Outline each Plasmodium falciparum-infected red blood cell.
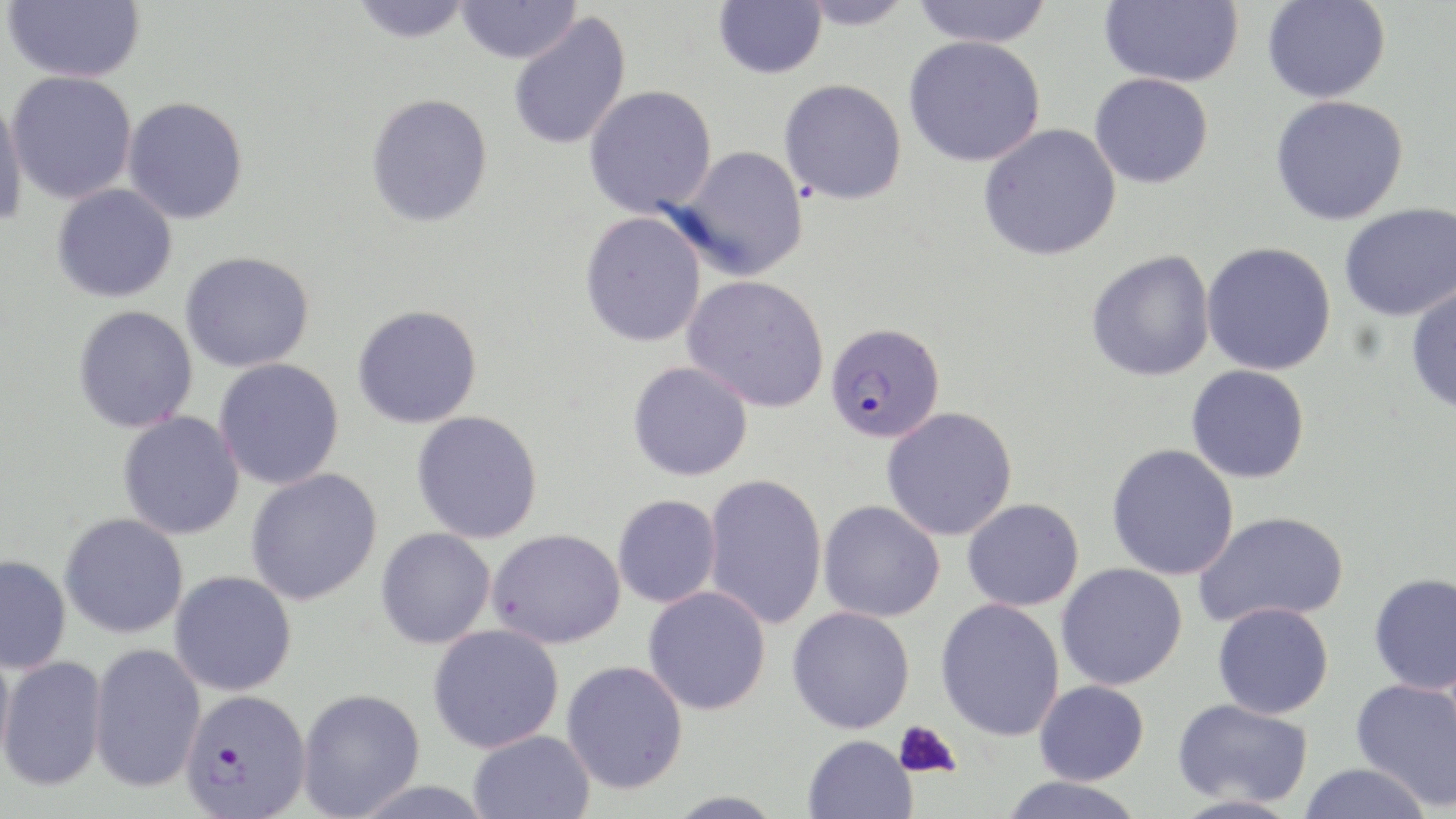

Approximate bounding boxes as [x1, y1, x2, y2] in pixels.
Plasmodium falciparum-infected red blood cells: [825, 321, 946, 444], [181, 688, 311, 816].

{
  "slide_level_diagnosis": "Plasmodium falciparum",
  "uninfected_red_blood_cell_locations": "approximate bounding boxes as [x1, y1, x2, y2] in pixels: [2, 0, 145, 83], [350, 0, 472, 42], [455, 0, 581, 64], [714, 0, 826, 79], [796, 0, 915, 30], [912, 0, 1053, 48], [1098, 0, 1243, 88], [1262, 1, 1390, 103], [508, 13, 631, 151], [903, 35, 1046, 167], [6, 71, 137, 204], [1088, 73, 1213, 189], [779, 78, 907, 205], [584, 85, 717, 218], [0, 92, 27, 232], [366, 93, 493, 228], [1270, 95, 1410, 226], [122, 96, 248, 224], [978, 123, 1121, 262], [672, 144, 810, 281], [51, 184, 177, 303], [1339, 202, 1455, 322], [580, 211, 707, 348], [1201, 242, 1337, 375], [1086, 250, 1215, 382], [180, 251, 315, 372], [682, 274, 829, 412], [1405, 284, 1456, 415], [352, 304, 483, 428], [73, 305, 198, 433], [213, 358, 345, 490], [627, 361, 753, 481], [1186, 364, 1310, 483], [882, 407, 1018, 541], [117, 410, 245, 540], [411, 411, 544, 543], [1106, 443, 1239, 580], [245, 468, 383, 605], [704, 473, 827, 630], [613, 494, 721, 607], [962, 498, 1084, 611], [818, 500, 945, 622], [1194, 511, 1348, 627], [59, 513, 188, 639], [375, 527, 496, 649], [487, 528, 625, 648], [0, 555, 71, 674], [1056, 563, 1187, 691], [170, 570, 297, 696], [1368, 573, 1456, 695], [642, 586, 771, 716], [935, 598, 1065, 741], [1212, 602, 1334, 719], [786, 606, 915, 734], [427, 624, 565, 753], [0, 638, 15, 775], [89, 642, 206, 793], [1, 655, 107, 791], [561, 660, 688, 795], [1350, 679, 1456, 811], [1034, 680, 1149, 785], [297, 688, 425, 818], [1172, 698, 1312, 807], [468, 730, 595, 819], [803, 734, 918, 819], [1298, 762, 1433, 819], [998, 776, 1147, 819], [666, 790, 786, 819]",
  "platelet_locations": "approximate bounding boxes as [x1, y1, x2, y2] in pixels: [894, 720, 961, 779]",
  "magnification": "1000x",
  "field_of_view": "one of a larger specimen",
  "stain": "May-Grünwald-Giemsa",
  "preparation": "thin blood film",
  "image_size": "1456×819 pixels",
  "modality": "light microscopy"
}